Name the parasite shown.
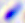
This is Toxoplasma gondii.

Micrograph. 400x magnification.